Locate every blood parasite and identify its species.
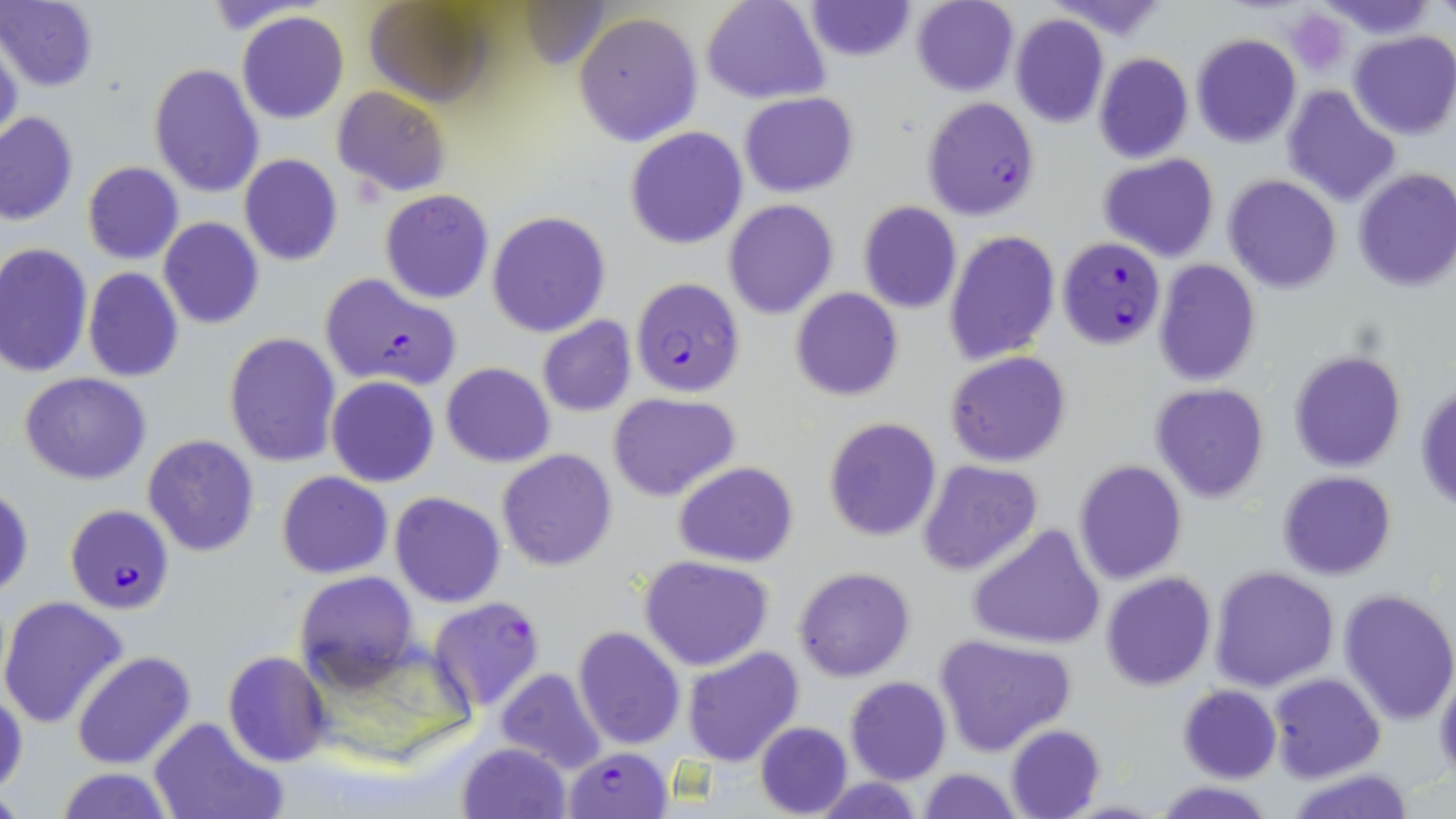
Approximate bounding boxes as (x1, y1, x2, y2) in pixels.
Plasmodium falciparum-infected red blood cells: (922, 96, 1041, 221), (1058, 236, 1166, 351), (319, 272, 462, 391), (630, 277, 745, 398), (64, 504, 175, 613), (428, 596, 546, 713), (567, 751, 672, 819).
No Plasmodium ovale, Plasmodium malariae, Plasmodium vivax, Babesia divergens, or Trypanosoma brucei observed.

Uninfected red blood cell locations: (362, 0, 497, 106), (701, 0, 830, 104), (803, 0, 917, 61), (910, 0, 1019, 97), (1323, 0, 1436, 36), (0, 1, 100, 91), (236, 11, 348, 123), (574, 12, 702, 147), (1009, 13, 1109, 127), (1349, 30, 1456, 139), (1191, 33, 1301, 148), (0, 38, 23, 152), (1092, 52, 1193, 164), (149, 63, 264, 197), (1281, 85, 1401, 207), (333, 86, 452, 196), (739, 91, 857, 198), (1, 111, 78, 226), (625, 126, 748, 249), (238, 154, 343, 266), (1098, 154, 1220, 262), (81, 161, 184, 265), (1352, 167, 1456, 293), (1223, 174, 1341, 293), (379, 189, 495, 305), (723, 201, 838, 319), (858, 202, 962, 315), (487, 210, 611, 338), (158, 217, 265, 329), (943, 230, 1060, 366), (0, 242, 94, 377), (1153, 259, 1260, 386), (82, 267, 185, 383), (790, 287, 902, 401), (537, 316, 636, 417), (223, 331, 341, 466), (1289, 350, 1406, 472), (945, 351, 1072, 468), (441, 362, 555, 467), (20, 372, 151, 485), (326, 375, 441, 487), (1416, 380, 1456, 515), (1150, 383, 1270, 502), (607, 391, 740, 501), (823, 416, 942, 541), (142, 434, 262, 558), (495, 449, 618, 571), (916, 458, 1043, 576), (1072, 459, 1188, 584), (674, 462, 800, 566), (1277, 470, 1397, 580), (276, 471, 393, 580), (1, 483, 35, 599), (389, 491, 505, 608), (966, 523, 1106, 651), (640, 556, 774, 672), (1212, 565, 1337, 692), (792, 566, 916, 682), (292, 570, 420, 692), (1101, 572, 1217, 692), (1337, 588, 1456, 726), (0, 594, 130, 729), (572, 626, 685, 750), (933, 635, 1078, 756), (680, 645, 805, 766), (222, 650, 334, 766), (71, 651, 196, 769), (1434, 663, 1456, 784), (495, 669, 610, 776), (1268, 673, 1384, 783), (844, 676, 951, 786), (0, 683, 26, 803), (1178, 685, 1281, 783), (147, 716, 286, 819), (756, 721, 854, 817), (1005, 724, 1106, 819), (456, 741, 572, 819), (54, 767, 176, 819), (1287, 767, 1418, 819), (916, 768, 1023, 818), (1151, 781, 1276, 817). Platelet locations: (1285, 8, 1350, 74). Slide-level diagnosis: Plasmodium falciparum. Captured at 1000x magnification. One field of a larger specimen. May-Grünwald-Giemsa stain. Optical microscopy. Thin blood film. Image is 1456×819 pixels.